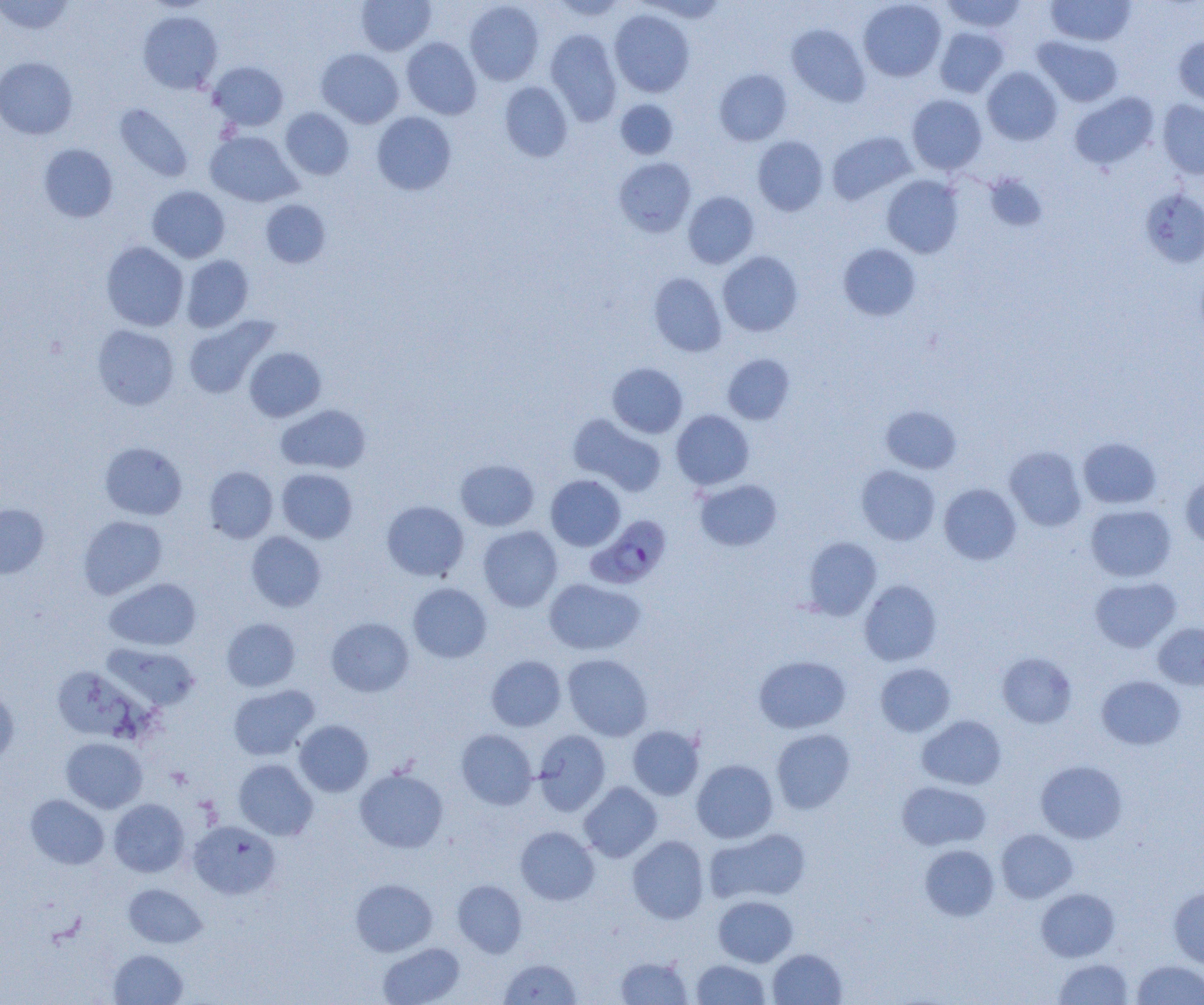
Approximate bounding boxes as named x1/y1/x2/y2 corners in pixels. Plasmodium falciparum-infected red blood cell locations: (x1=587, y1=515, x2=671, y2=589). Uninfected red blood cell locations: (x1=356, y1=0, x2=436, y2=55), (x1=551, y1=0, x2=628, y2=21), (x1=641, y1=0, x2=728, y2=23), (x1=859, y1=0, x2=946, y2=81), (x1=941, y1=0, x2=1026, y2=32), (x1=1046, y1=0, x2=1136, y2=47), (x1=0, y1=1, x2=75, y2=35), (x1=464, y1=1, x2=544, y2=85), (x1=609, y1=9, x2=695, y2=97), (x1=138, y1=11, x2=223, y2=94), (x1=786, y1=23, x2=870, y2=106), (x1=934, y1=26, x2=1009, y2=97), (x1=545, y1=29, x2=622, y2=125), (x1=1174, y1=35, x2=1204, y2=109), (x1=1032, y1=36, x2=1123, y2=107), (x1=402, y1=37, x2=482, y2=119), (x1=316, y1=48, x2=404, y2=128), (x1=0, y1=56, x2=78, y2=139), (x1=208, y1=61, x2=288, y2=131), (x1=982, y1=66, x2=1062, y2=145), (x1=714, y1=69, x2=792, y2=146), (x1=499, y1=81, x2=573, y2=161), (x1=1070, y1=92, x2=1158, y2=170), (x1=907, y1=94, x2=987, y2=174), (x1=615, y1=99, x2=678, y2=159), (x1=1158, y1=100, x2=1204, y2=179), (x1=114, y1=104, x2=193, y2=182), (x1=280, y1=108, x2=354, y2=180), (x1=372, y1=111, x2=456, y2=195), (x1=205, y1=131, x2=301, y2=207), (x1=827, y1=131, x2=916, y2=204), (x1=753, y1=135, x2=828, y2=216), (x1=38, y1=143, x2=118, y2=222), (x1=614, y1=157, x2=696, y2=237), (x1=985, y1=174, x2=1047, y2=232), (x1=882, y1=175, x2=963, y2=258), (x1=147, y1=186, x2=230, y2=263), (x1=1139, y1=188, x2=1204, y2=268), (x1=683, y1=191, x2=759, y2=268), (x1=260, y1=199, x2=331, y2=268), (x1=101, y1=241, x2=189, y2=331), (x1=838, y1=243, x2=921, y2=321), (x1=717, y1=251, x2=803, y2=336), (x1=181, y1=255, x2=253, y2=332), (x1=649, y1=272, x2=727, y2=356), (x1=182, y1=315, x2=279, y2=399), (x1=92, y1=325, x2=179, y2=409), (x1=244, y1=347, x2=326, y2=422), (x1=722, y1=353, x2=794, y2=424), (x1=607, y1=363, x2=687, y2=438), (x1=276, y1=404, x2=371, y2=474), (x1=881, y1=405, x2=961, y2=474), (x1=671, y1=410, x2=754, y2=490), (x1=567, y1=413, x2=667, y2=496), (x1=1078, y1=437, x2=1161, y2=508), (x1=99, y1=442, x2=187, y2=520), (x1=1005, y1=446, x2=1086, y2=531), (x1=455, y1=459, x2=539, y2=531), (x1=204, y1=466, x2=278, y2=543), (x1=856, y1=466, x2=940, y2=545), (x1=277, y1=468, x2=357, y2=543), (x1=857, y1=474, x2=1020, y2=549), (x1=545, y1=475, x2=625, y2=551), (x1=1180, y1=475, x2=1204, y2=548), (x1=695, y1=479, x2=782, y2=551), (x1=939, y1=483, x2=1021, y2=565), (x1=381, y1=500, x2=469, y2=581), (x1=0, y1=504, x2=49, y2=579), (x1=1086, y1=504, x2=1176, y2=581), (x1=78, y1=515, x2=168, y2=599), (x1=478, y1=526, x2=563, y2=612), (x1=246, y1=531, x2=327, y2=612), (x1=803, y1=537, x2=882, y2=620), (x1=1090, y1=576, x2=1181, y2=653), (x1=104, y1=578, x2=201, y2=651), (x1=544, y1=578, x2=645, y2=655), (x1=859, y1=580, x2=942, y2=666), (x1=408, y1=582, x2=491, y2=662), (x1=326, y1=617, x2=414, y2=697), (x1=221, y1=618, x2=300, y2=692), (x1=1153, y1=623, x2=1204, y2=690), (x1=104, y1=643, x2=201, y2=711), (x1=996, y1=651, x2=1077, y2=728), (x1=562, y1=654, x2=653, y2=741), (x1=485, y1=655, x2=566, y2=731), (x1=754, y1=655, x2=851, y2=733), (x1=875, y1=663, x2=955, y2=736), (x1=1096, y1=675, x2=1186, y2=750), (x1=228, y1=684, x2=319, y2=760), (x1=0, y1=685, x2=19, y2=765), (x1=917, y1=715, x2=1006, y2=790), (x1=294, y1=720, x2=373, y2=797), (x1=627, y1=725, x2=704, y2=800), (x1=771, y1=728, x2=855, y2=813), (x1=456, y1=729, x2=537, y2=809), (x1=533, y1=730, x2=610, y2=815), (x1=61, y1=738, x2=147, y2=813), (x1=233, y1=759, x2=318, y2=840), (x1=691, y1=759, x2=778, y2=843), (x1=1035, y1=760, x2=1127, y2=843), (x1=355, y1=767, x2=448, y2=853), (x1=897, y1=781, x2=991, y2=851), (x1=579, y1=782, x2=662, y2=862), (x1=26, y1=794, x2=108, y2=869), (x1=109, y1=799, x2=189, y2=877), (x1=188, y1=821, x2=280, y2=899), (x1=515, y1=826, x2=599, y2=904), (x1=706, y1=828, x2=811, y2=904), (x1=996, y1=829, x2=1077, y2=902), (x1=627, y1=835, x2=709, y2=924), (x1=919, y1=839, x2=1077, y2=911), (x1=919, y1=844, x2=999, y2=921), (x1=350, y1=878, x2=438, y2=956), (x1=452, y1=879, x2=527, y2=957), (x1=123, y1=883, x2=207, y2=948), (x1=1168, y1=886, x2=1204, y2=970), (x1=1036, y1=888, x2=1120, y2=961), (x1=713, y1=895, x2=797, y2=967), (x1=378, y1=942, x2=465, y2=1005), (x1=768, y1=948, x2=847, y2=1005), (x1=109, y1=949, x2=187, y2=1005), (x1=615, y1=956, x2=693, y2=1004), (x1=1053, y1=957, x2=1134, y2=1004), (x1=499, y1=958, x2=582, y2=1004), (x1=691, y1=959, x2=771, y2=1004), (x1=1131, y1=960, x2=1204, y2=1004). Slide-level diagnosis: Plasmodium falciparum. Thin blood smear. Light microscopy. Captured at 1000x magnification. Image is 1204×1005 pixels. One field of a larger specimen.